Outline each Plasmodium ovale-infected red blood cell.
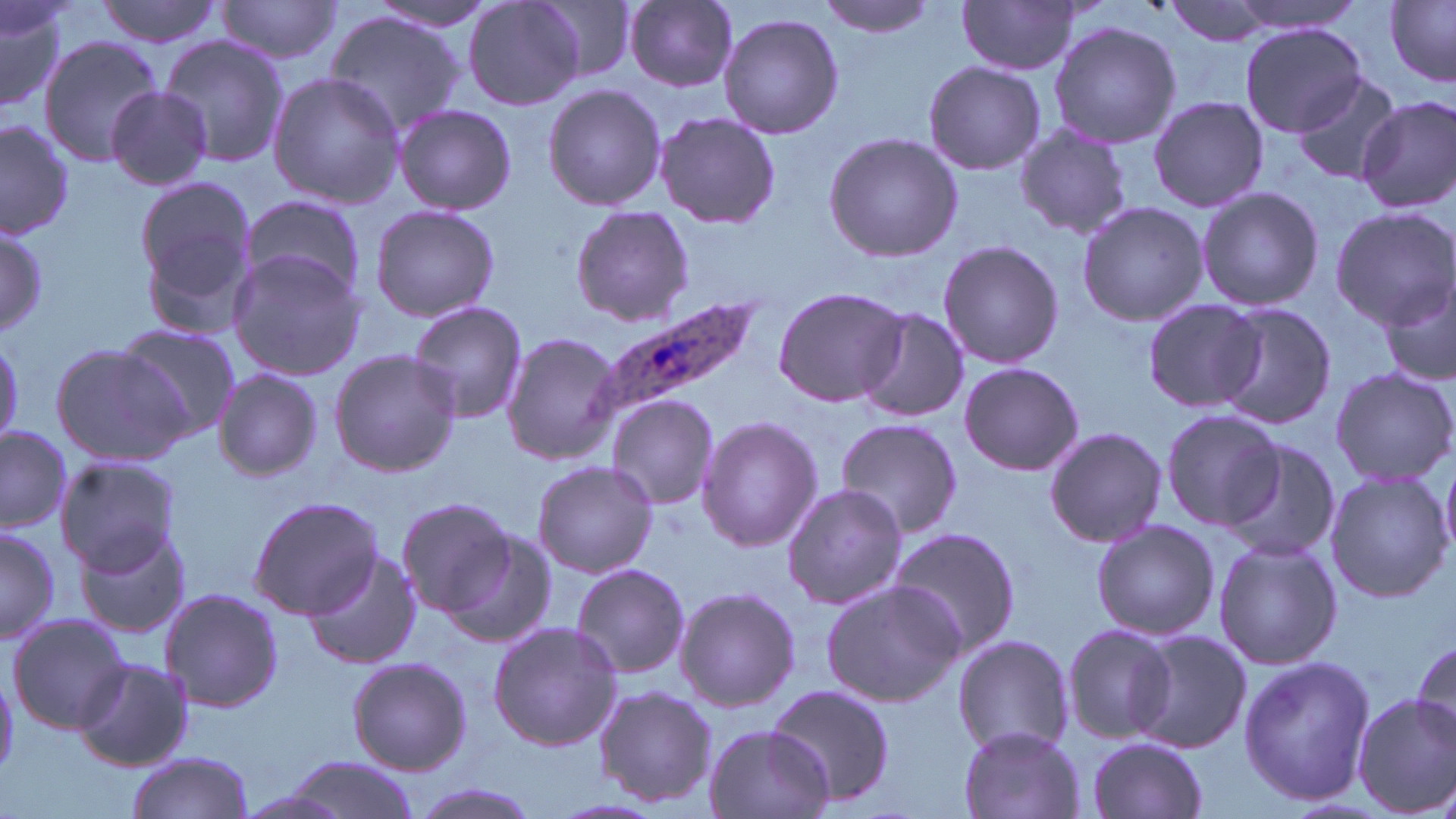
Approximate bounding boxes as (x1, y1, x2, y2) in pixels.
Plasmodium ovale-infected red blood cells: (587, 295, 770, 428).

Uninfected red blood cell locations: (0, 0, 70, 113), (95, 0, 224, 48), (216, 0, 341, 63), (463, 0, 583, 111), (817, 0, 942, 37), (958, 0, 1083, 75), (1220, 0, 1369, 38), (364, 1, 496, 32), (534, 1, 638, 82), (624, 1, 737, 90), (1161, 1, 1282, 46), (1386, 2, 1456, 85), (325, 10, 465, 136), (718, 12, 845, 139), (1048, 21, 1179, 149), (1237, 23, 1372, 136), (156, 36, 291, 170), (38, 37, 161, 167), (923, 60, 1048, 175), (1290, 71, 1404, 185), (266, 72, 406, 210), (541, 82, 667, 211), (103, 86, 212, 191), (1149, 96, 1268, 212), (1356, 97, 1456, 214), (394, 104, 516, 214), (654, 112, 781, 227), (0, 117, 75, 242), (1012, 124, 1135, 242), (823, 131, 962, 263), (132, 176, 260, 325), (1195, 186, 1324, 312), (236, 194, 368, 301), (1076, 202, 1208, 326), (367, 204, 501, 322), (571, 205, 694, 325), (1329, 207, 1456, 328), (0, 218, 46, 344), (937, 239, 1063, 370), (226, 250, 366, 379), (1379, 275, 1456, 385), (771, 286, 911, 408), (1141, 295, 1268, 415), (405, 299, 529, 426), (1214, 304, 1338, 429), (852, 309, 971, 425), (115, 323, 240, 437), (502, 332, 621, 465), (0, 339, 27, 440), (51, 342, 196, 462), (328, 349, 461, 477), (958, 362, 1083, 476), (1329, 366, 1456, 488), (213, 367, 323, 483), (608, 397, 719, 510), (1159, 408, 1284, 532), (696, 415, 822, 552), (834, 418, 964, 538), (0, 424, 73, 533), (1045, 427, 1168, 546), (1220, 437, 1342, 564), (1440, 454, 1456, 563), (54, 455, 182, 573), (531, 460, 659, 577), (1323, 470, 1452, 604), (782, 483, 909, 610), (248, 495, 383, 618), (395, 497, 519, 617), (74, 518, 191, 638), (1090, 518, 1218, 641), (0, 523, 60, 643), (886, 526, 1021, 656), (446, 532, 557, 650), (1212, 538, 1342, 670), (304, 550, 421, 669), (570, 562, 691, 680), (819, 580, 963, 707), (674, 585, 800, 713), (160, 587, 284, 714), (6, 612, 129, 733), (487, 621, 623, 753), (1060, 623, 1175, 746), (1127, 628, 1251, 755), (951, 634, 1073, 755), (1409, 638, 1456, 745), (1237, 653, 1375, 806), (73, 657, 193, 771), (346, 657, 472, 774), (592, 684, 717, 809), (766, 684, 896, 806), (1352, 694, 1456, 817), (704, 724, 836, 819), (958, 726, 1085, 818), (1086, 736, 1207, 818), (125, 753, 255, 818), (281, 755, 420, 819), (406, 782, 546, 819), (234, 789, 353, 819). Slide-level diagnosis: Plasmodium ovale. 1000x magnification. Thin blood smear. May-Grünwald-Giemsa-stained preparation. Image is 1456×819 pixels. Light microscopy. Single field of view.